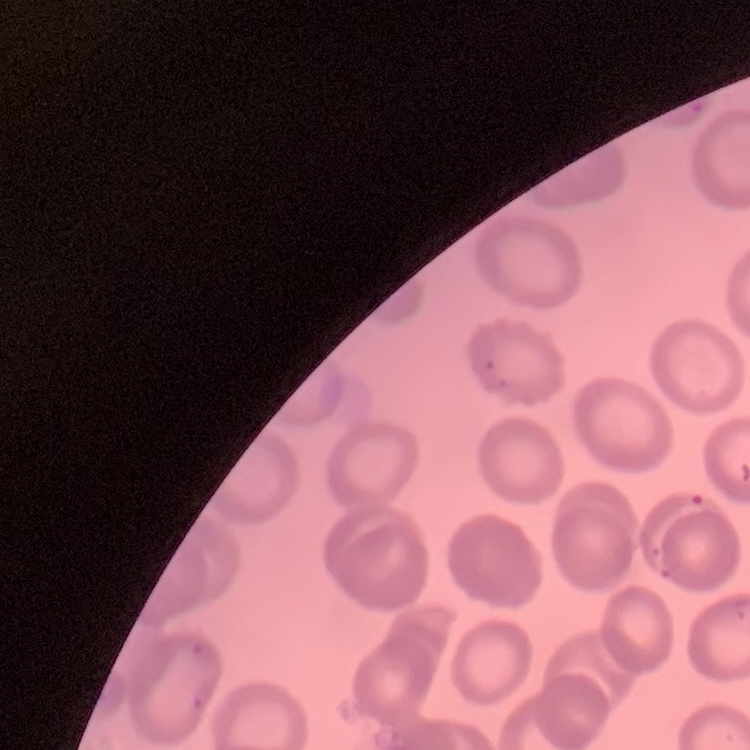

erythrocyte_morphology: no rouleaux formation
preparation: thin blood smear
stain: Field's or Giemsa
image_type: square crop of a larger photomicrograph